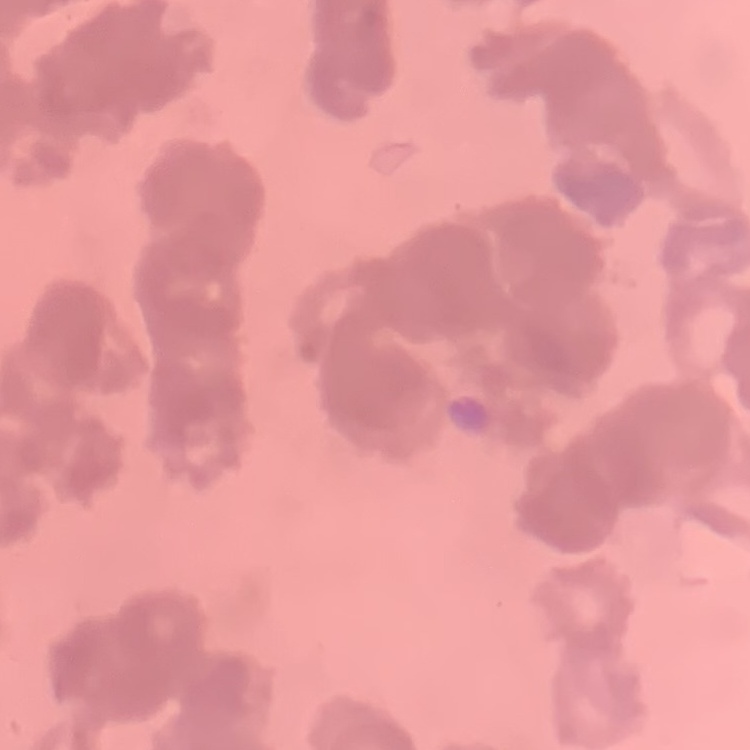
{
  "erythrocyte_morphology": "rouleaux formation",
  "stain": "Field's or Giemsa",
  "preparation": "thin blood film",
  "image_type": "square crop of a larger photomicrograph"
}